State which cell type is depicted.
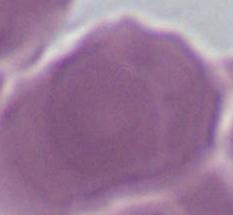
An erythrocyte.

1000x magnification. Micrograph.